Locate every blood parasite and identify its species.
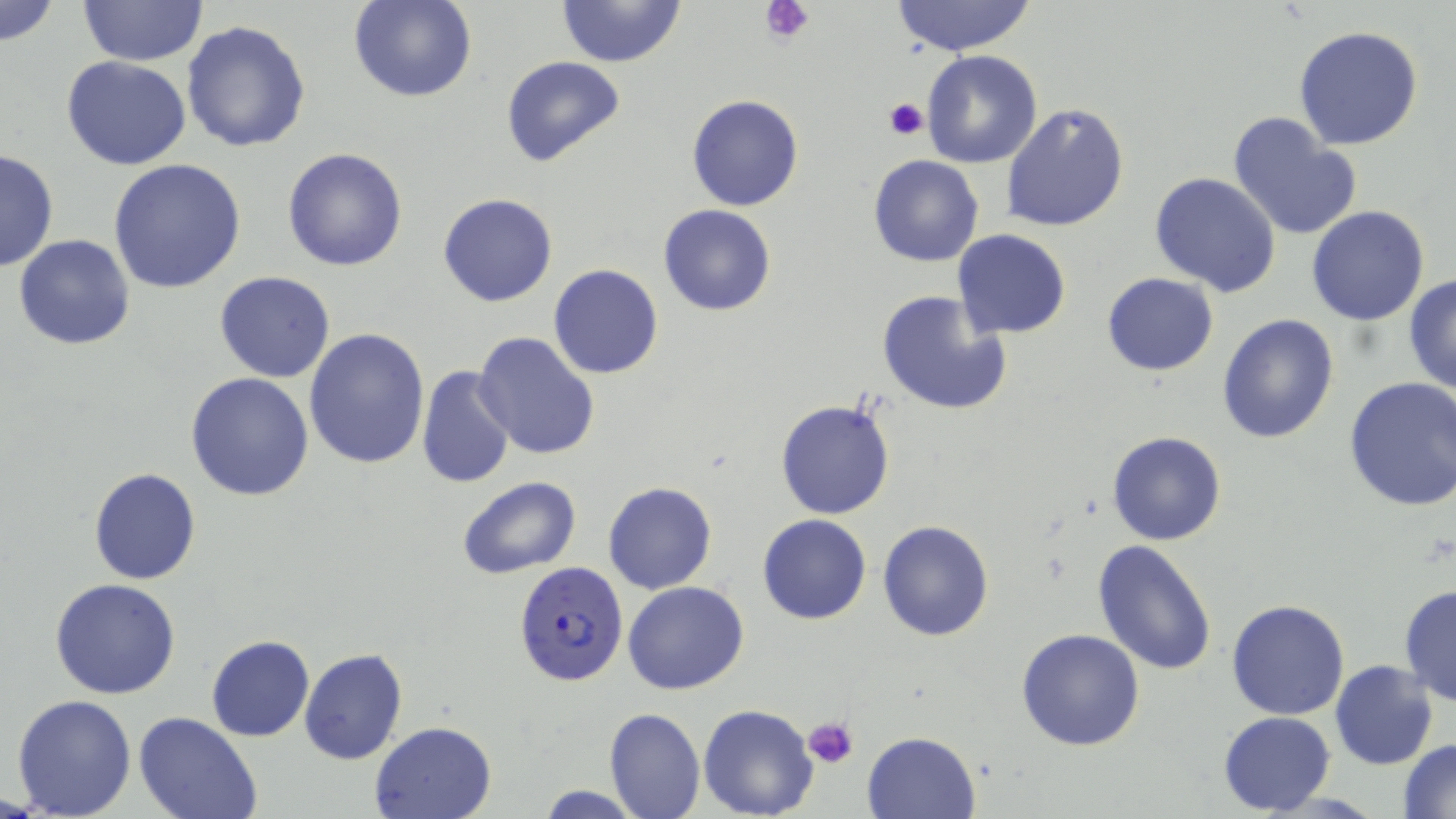
Approximate bounding boxes as (x1,y1)-(x2,y2) corner pairs in pixels.
Plasmodium falciparum-infected red blood cells: (514,559)-(630,689).
No Plasmodium ovale, Plasmodium malariae, Plasmodium vivax, Babesia divergens, or Trypanosoma brucei observed.

{
  "slide_level_diagnosis": "Plasmodium falciparum",
  "stain": "May-Grünwald-Giemsa",
  "modality": "light microscopy",
  "uninfected_red_blood_cell_locations": "approximate bounding boxes as (x1,y1)-(x2,y2) corner pairs in pixels: (0,0)-(61,49), (78,0)-(206,67), (350,0)-(475,103), (557,0)-(687,68), (890,0)-(1038,57), (181,20)-(312,154), (1294,25)-(1424,150), (920,51)-(1043,169), (62,56)-(192,170), (501,56)-(626,169), (686,95)-(804,211), (1002,102)-(1129,233), (1228,111)-(1363,243), (282,147)-(408,272), (1,149)-(59,273), (868,155)-(984,268), (108,158)-(247,294), (1150,172)-(1281,296), (438,193)-(558,307), (659,204)-(776,316), (1306,205)-(1431,325), (952,229)-(1072,339), (14,234)-(135,350), (548,264)-(663,380), (214,271)-(337,383), (1101,272)-(1218,376), (1404,272)-(1456,397), (876,289)-(1013,417), (1216,312)-(1340,444), (304,329)-(431,470), (473,332)-(601,462), (416,365)-(515,487), (185,373)-(315,501), (1342,377)-(1456,511), (773,397)-(896,521), (1107,431)-(1227,546), (88,468)-(200,584), (456,474)-(582,579), (612,478)-(731,693), (603,481)-(716,594), (757,514)-(871,624), (877,520)-(994,642), (1092,538)-(1219,674), (49,578)-(183,699), (623,581)-(749,695), (1398,583)-(1456,706), (1226,599)-(1349,719), (1016,628)-(1146,751), (206,635)-(314,741), (299,648)-(408,765), (1330,660)-(1438,769), (10,694)-(138,818), (698,703)-(819,819), (604,707)-(705,818), (1218,711)-(1335,816), (134,712)-(261,819), (367,720)-(497,819), (862,730)-(982,819), (1398,739)-(1456,817), (533,786)-(647,817)",
  "image_size": "1456×819 pixels",
  "platelet_locations": "approximate bounding boxes as (x1,y1)-(x2,y2) corner pairs in pixels: (762,0)-(814,44), (884,97)-(928,140), (803,715)-(859,768)",
  "field_of_view": "one of a larger specimen",
  "preparation": "thin blood film",
  "magnification": "1000x"
}